Identify the blood parasite species.
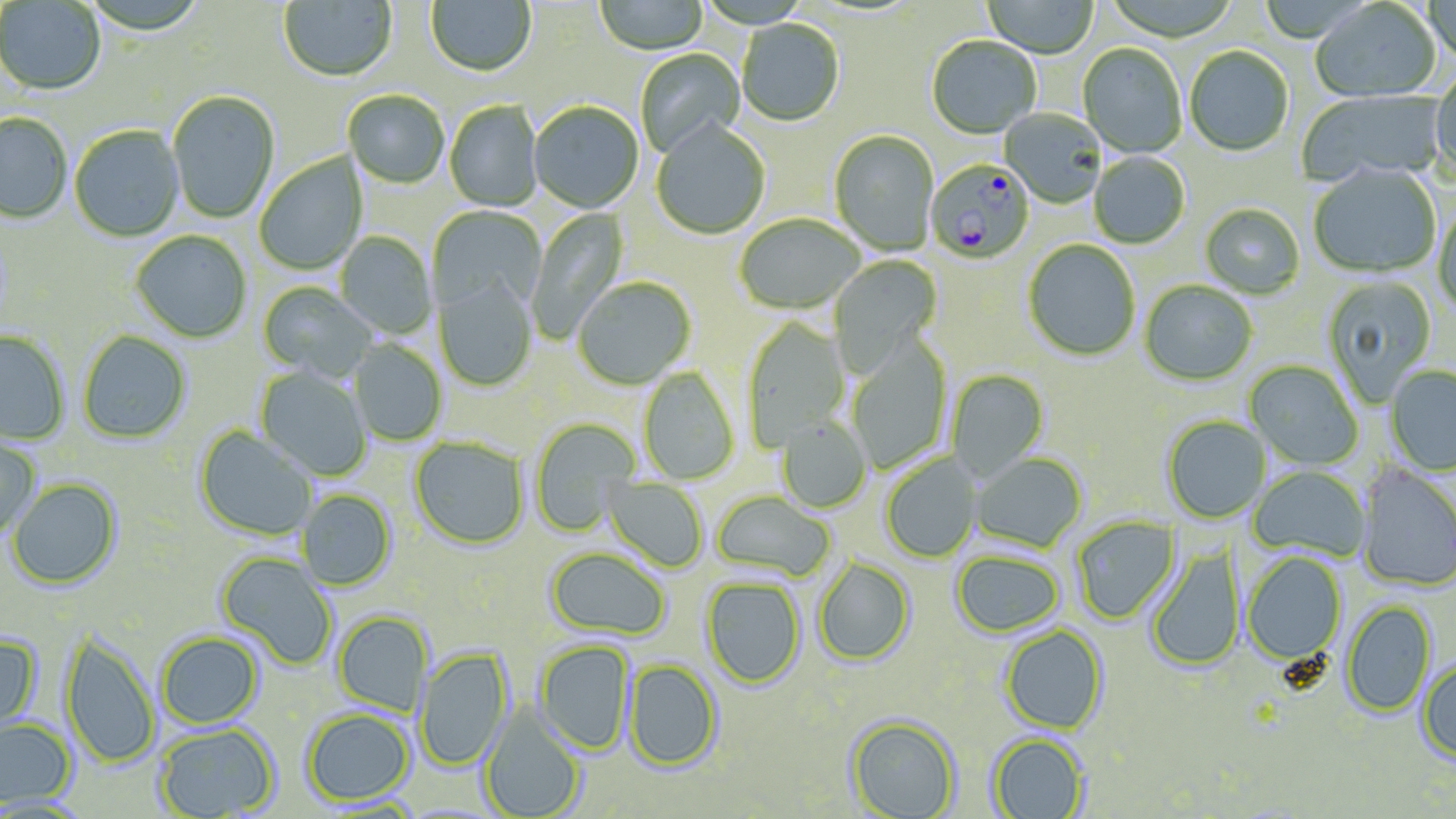

Plasmodium falciparum.

Approximate bounding boxes as (x1, y1, x2, y2) in pixels. Plasmodium falciparum-infected red blood cell locations: (924, 160, 1035, 266). Uninfected red blood cell locations: (278, 0, 397, 83), (425, 0, 537, 79), (594, 0, 708, 57), (1422, 0, 1456, 71), (0, 1, 105, 96), (981, 1, 1100, 59), (1309, 1, 1442, 104), (736, 21, 845, 129), (926, 37, 1041, 141), (1078, 44, 1187, 159), (1184, 47, 1294, 157), (634, 49, 746, 160), (1430, 76, 1456, 183), (1297, 89, 1447, 188), (167, 91, 280, 224), (343, 91, 450, 190), (444, 101, 543, 212), (528, 102, 644, 215), (1000, 109, 1107, 209), (0, 113, 73, 225), (651, 123, 770, 240), (69, 126, 185, 242), (829, 131, 939, 256), (1088, 152, 1190, 250), (254, 153, 367, 275), (1308, 165, 1441, 279), (1432, 204, 1456, 320), (1199, 205, 1305, 299), (428, 206, 547, 317), (527, 206, 631, 343), (734, 215, 864, 317), (130, 231, 252, 344), (334, 232, 437, 339), (1023, 240, 1140, 362), (828, 255, 943, 379), (1320, 275, 1437, 407), (433, 277, 538, 392), (572, 279, 696, 391), (1139, 281, 1257, 387), (258, 282, 377, 383), (742, 318, 851, 451), (0, 330, 70, 445), (77, 331, 192, 444), (846, 337, 952, 473), (349, 340, 447, 446), (1243, 360, 1364, 470), (254, 365, 372, 482), (1384, 366, 1456, 476), (638, 367, 740, 485), (945, 370, 1050, 482), (1163, 416, 1272, 524), (530, 417, 640, 537), (776, 417, 872, 513), (194, 426, 317, 543), (0, 435, 41, 537), (409, 437, 530, 551), (970, 453, 1087, 553), (880, 454, 982, 564), (1248, 465, 1370, 561), (1356, 465, 1456, 592), (601, 476, 709, 573), (7, 478, 123, 590), (297, 490, 397, 591), (710, 491, 836, 584), (1071, 515, 1181, 624), (1146, 546, 1246, 672), (544, 547, 671, 642), (950, 550, 1066, 638), (216, 552, 338, 671), (1242, 552, 1347, 665), (813, 557, 916, 667), (700, 576, 806, 690), (1340, 601, 1437, 717), (333, 610, 433, 716), (999, 625, 1108, 734), (59, 631, 160, 768), (156, 631, 264, 729), (0, 634, 43, 738), (534, 640, 636, 755), (415, 647, 513, 772), (623, 659, 723, 772), (1416, 659, 1456, 765), (478, 703, 587, 818), (302, 708, 415, 806), (846, 715, 961, 819), (0, 718, 78, 808), (153, 723, 280, 818), (988, 733, 1090, 819). Image is 1456×819 pixels. Single field of view. 1000x magnification. Thin blood smear. Light microscopy. May-Grünwald-Giemsa-stained preparation.